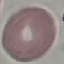
Result: negative for malaria parasites. Giemsa-stained preparation. Acquired by smartphone through the microscope eyepiece. Thin smear of blood. Automatically extracted cell patch, resized to 64 × 64 pixels.